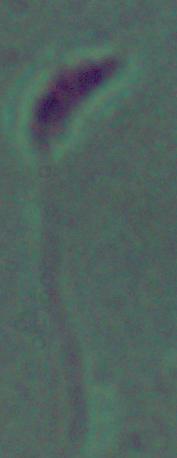

Micrograph. A Leishmania parasite is shown. 1000x magnification.